Describe the morphology of the erythrocytes.
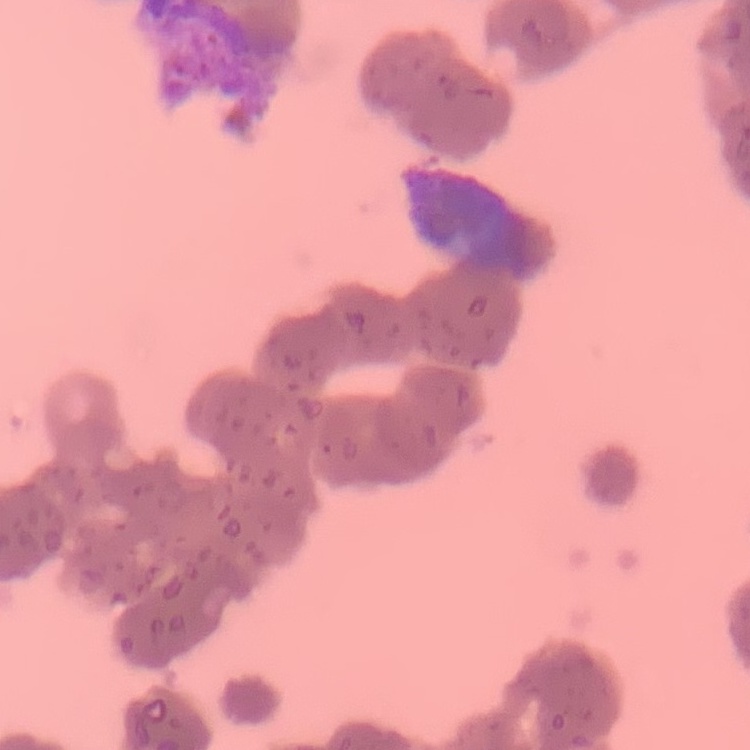
Rouleaux formation.

Summary:
  - Preparation: thin blood film
  - Stain: Field's or Giemsa
  - Image type: square crop of a larger photomicrograph